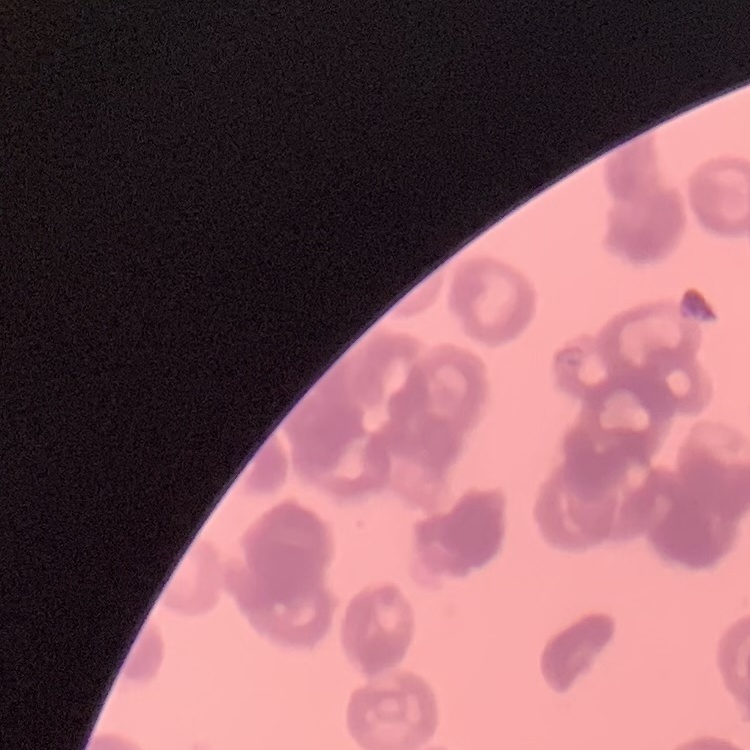

red blood cell morphology = rouleaux formation
preparation = thin peripheral smear
stain = Field's or Giemsa
image type = square crop of a larger photomicrograph